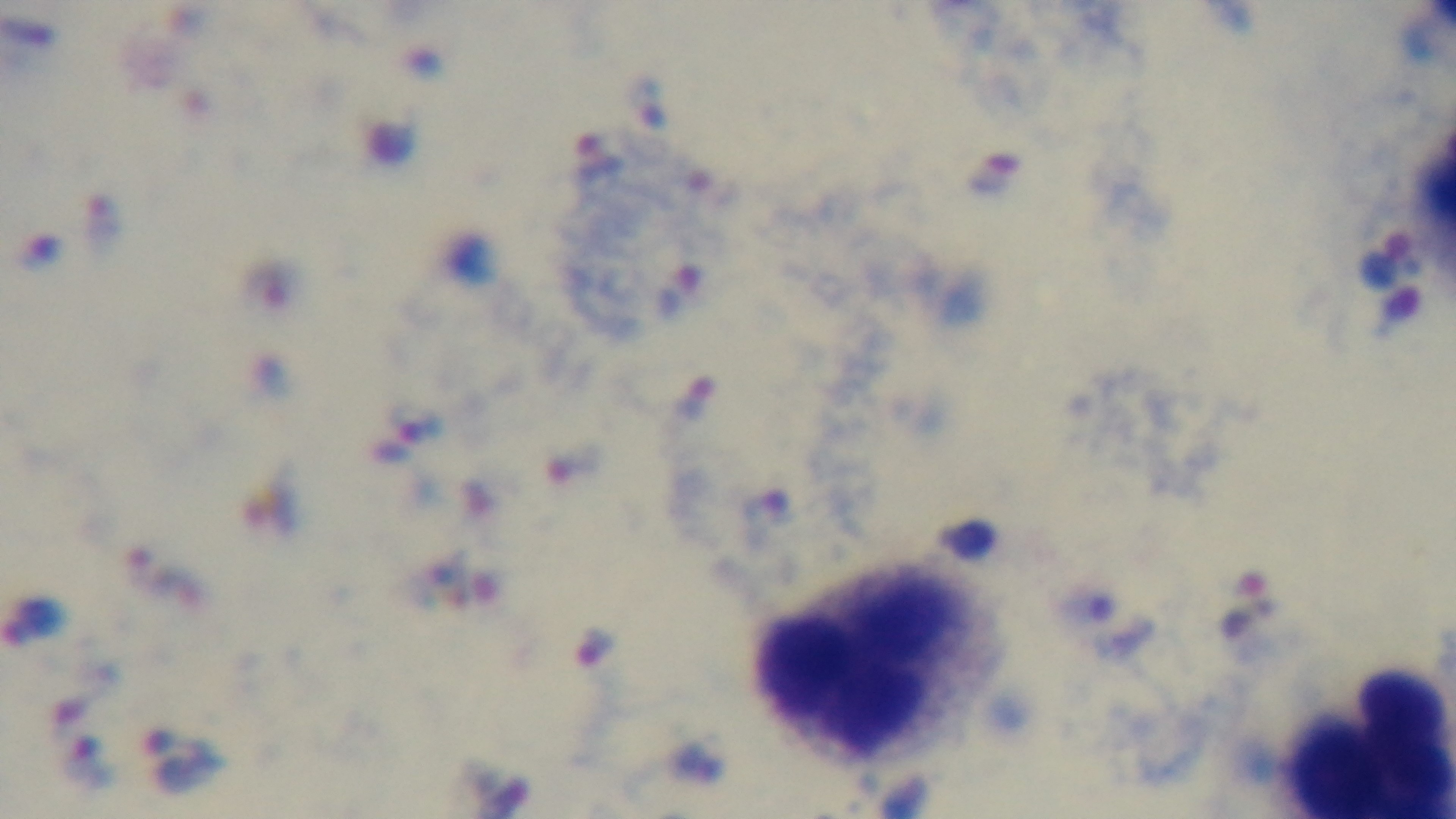

Summary:
  - Capture: mounted 4K digital camera
  - Stain: Giemsa
  - Modality: light microscopy
  - Field of view: single
  - Malaria status: positive
  - Objective: 100x oil immersion
  - Preparation: thick